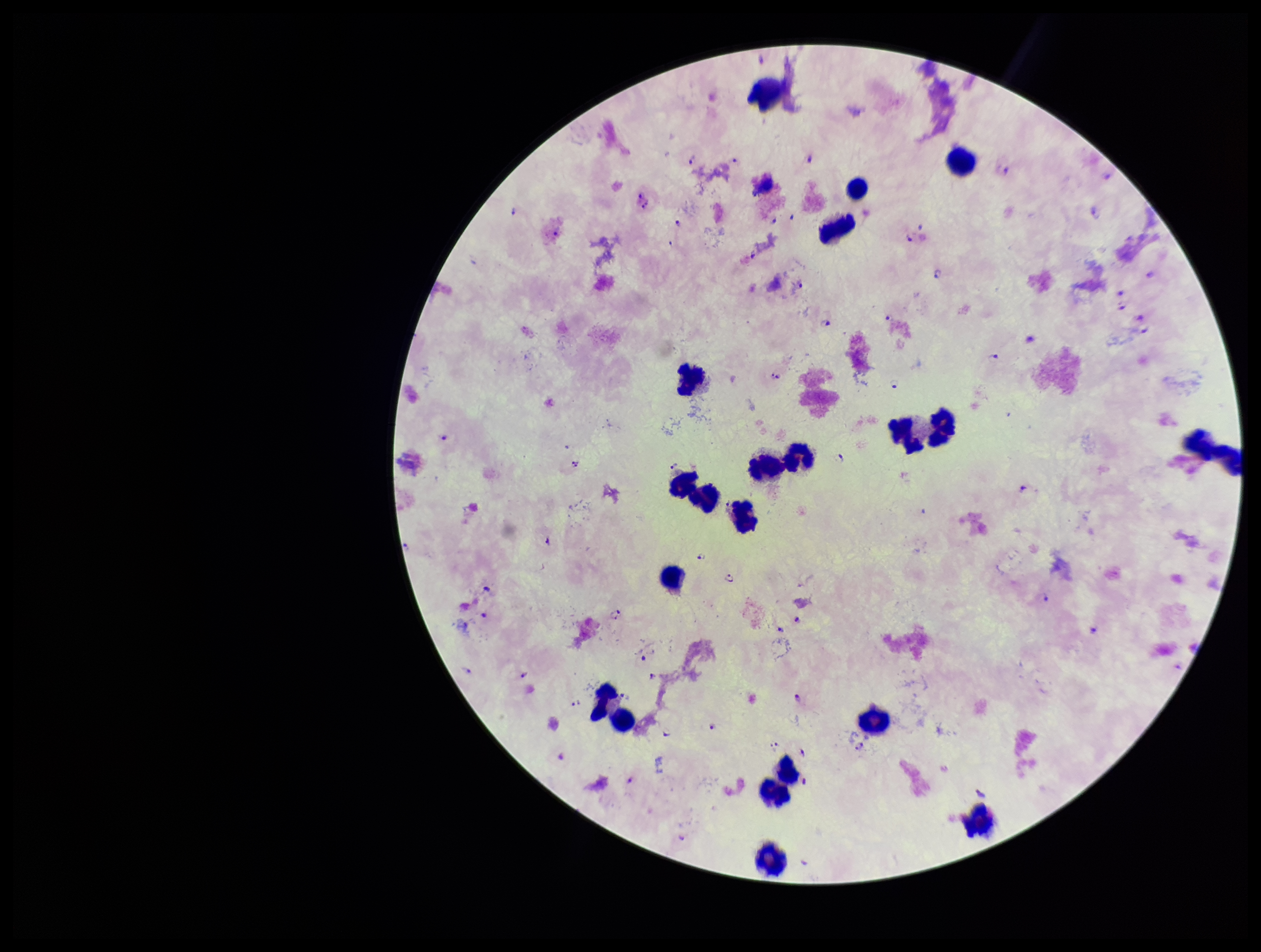

field of view = single
capture = smartphone photograph through the microscope eyepiece
Plasmodium parasites = identified
species reported for this patient = Plasmodium falciparum
leukocyte count = 20
image size = 1261×952 pixels
stain = Giemsa
preparation = thick smear
patient malaria status = infected
parasite count = 53